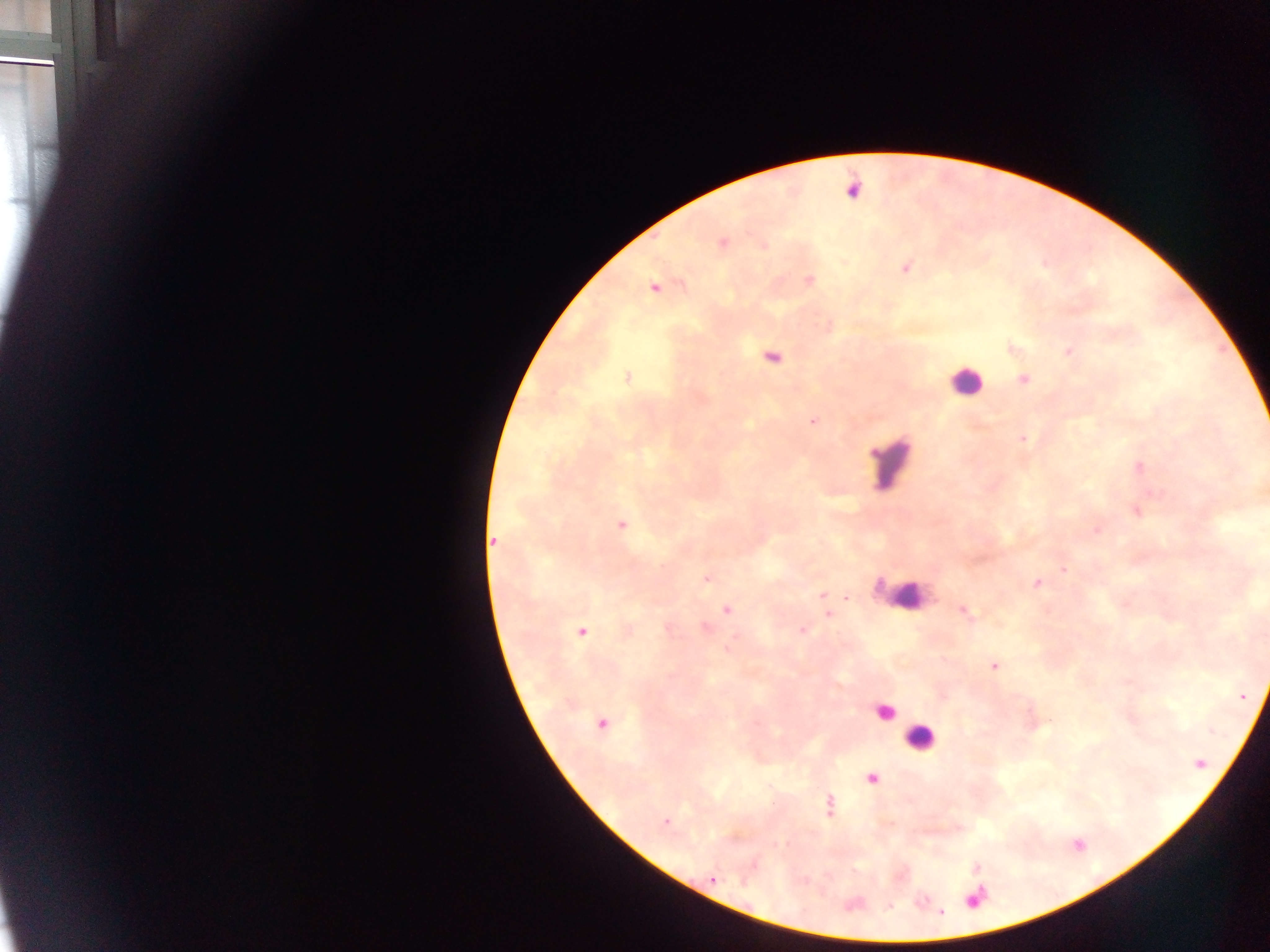

Approximate centers as [x, y] in pixels. Plasmodium parasite locations: [853, 188], [723, 243], [763, 246], [906, 268], [810, 280], [654, 287], [1069, 351], [772, 357], [627, 377], [1024, 380], [812, 421], [1022, 439], [1140, 468], [621, 525], [1096, 530], [493, 540], [1063, 569], [707, 579], [1037, 583], [822, 595], [727, 610], [963, 612], [828, 613], [706, 627], [802, 629], [582, 632], [994, 667], [1241, 696], [601, 723], [1200, 764], [872, 779], [829, 805], [665, 822], [712, 879], [980, 897], [941, 912]. Leukocyte locations: [965, 380], [891, 461], [908, 595], [885, 712], [921, 738]. Sample from Ghana. Thick blood smear. One field of view. Image is 1270×952 pixels. Photographed through a microscope with a mobile-phone camera.